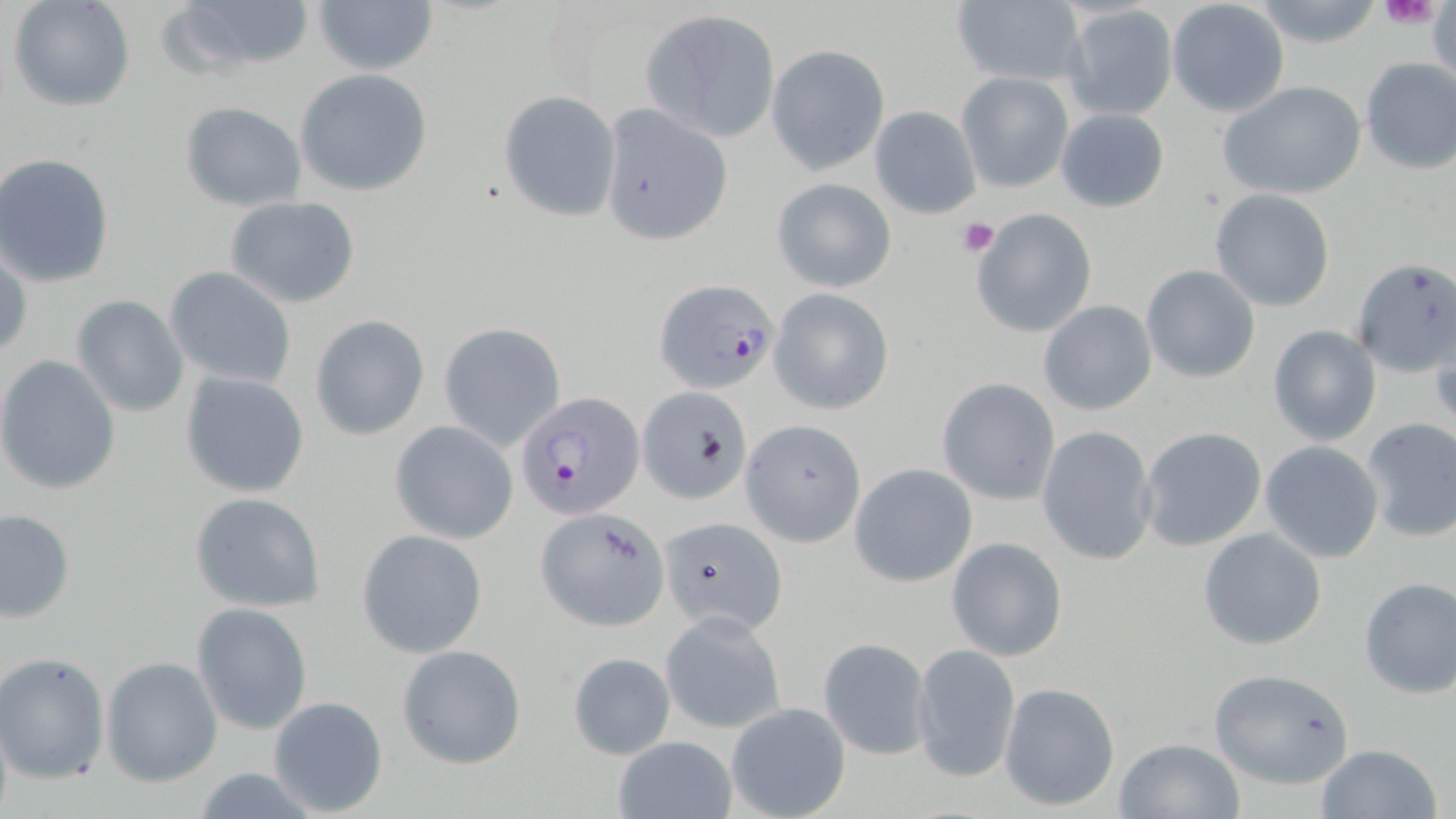 Approximate bounding boxes as (x1,y1)-(x2,y2) corner pairs in pixels. Uninfected red blood cell locations: (8,0)-(134,113), (161,0)-(318,81), (950,0)-(1085,87), (1250,0)-(1388,50), (311,1)-(438,77), (1167,1)-(1289,117), (1062,6)-(1177,122), (641,9)-(780,142), (765,44)-(890,175), (1358,57)-(1456,175), (295,69)-(432,197), (955,72)-(1073,193), (1219,82)-(1365,201), (498,90)-(622,221), (179,101)-(307,211), (598,105)-(733,246), (870,105)-(982,219), (1055,108)-(1169,212), (2,155)-(118,288), (771,177)-(897,293), (1209,189)-(1336,312), (224,195)-(362,308), (971,209)-(1098,338), (0,244)-(31,364), (1351,259)-(1455,378), (1140,265)-(1261,383), (164,266)-(297,388), (769,289)-(894,414), (70,294)-(190,418), (1039,301)-(1156,416), (309,314)-(430,440), (438,323)-(565,449), (1428,323)-(1456,427), (1267,324)-(1381,446), (0,355)-(123,495), (180,371)-(310,498), (936,378)-(1059,503), (639,386)-(754,505), (1358,417)-(1456,542), (742,419)-(866,546), (390,420)-(518,543), (1036,425)-(1158,566), (1138,425)-(1269,553), (1259,441)-(1385,564), (849,463)-(978,586), (189,490)-(326,612), (536,507)-(669,630), (1,508)-(75,623), (658,515)-(789,637), (1197,527)-(1328,651), (358,529)-(486,655), (946,537)-(1068,661), (1357,576)-(1456,699), (191,602)-(312,735), (660,612)-(786,734), (817,636)-(932,761), (911,643)-(1021,783), (396,644)-(527,770), (0,651)-(110,785), (566,651)-(675,760), (101,655)-(222,786), (1207,667)-(1357,789), (999,681)-(1121,812), (266,695)-(389,817), (724,701)-(851,819), (0,709)-(13,819), (612,735)-(735,818), (1115,737)-(1245,818), (1313,744)-(1444,819). Plasmodium falciparum-infected red blood cell locations: (653,276)-(780,394), (514,392)-(645,519). Platelet locations: (1381,0)-(1442,30), (956,218)-(999,257). Slide-level diagnosis: Plasmodium falciparum. Optical microscopy. 1000x magnification. One field of a larger specimen. Image is 1456×819 pixels. May-Grünwald-Giemsa stain. Thin blood film.